Assess this cell for malaria.
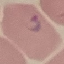

Parasitized.

Summary:
  - Stain: Giemsa
  - Preparation: thin blood smear
  - Image type: cell patch, automatically extracted from a larger field of view and resized to 64 × 64 pixels
  - Capture: smartphone camera at the microscope eyepiece